Report the malaria status of this cell.
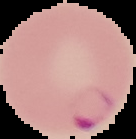
It is parasitized.

{
  "preparation": "thin blood smear",
  "image_type": "segmented cell region on a black background",
  "image_size": "136×139 pixels"
}